Name the parasite shown.
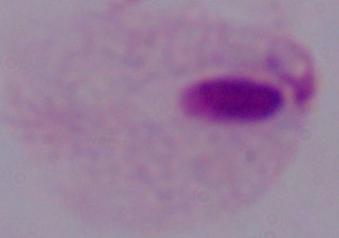

A trichomonad.

modality: photomicrograph
magnification: 1000x